Assess for malaria.
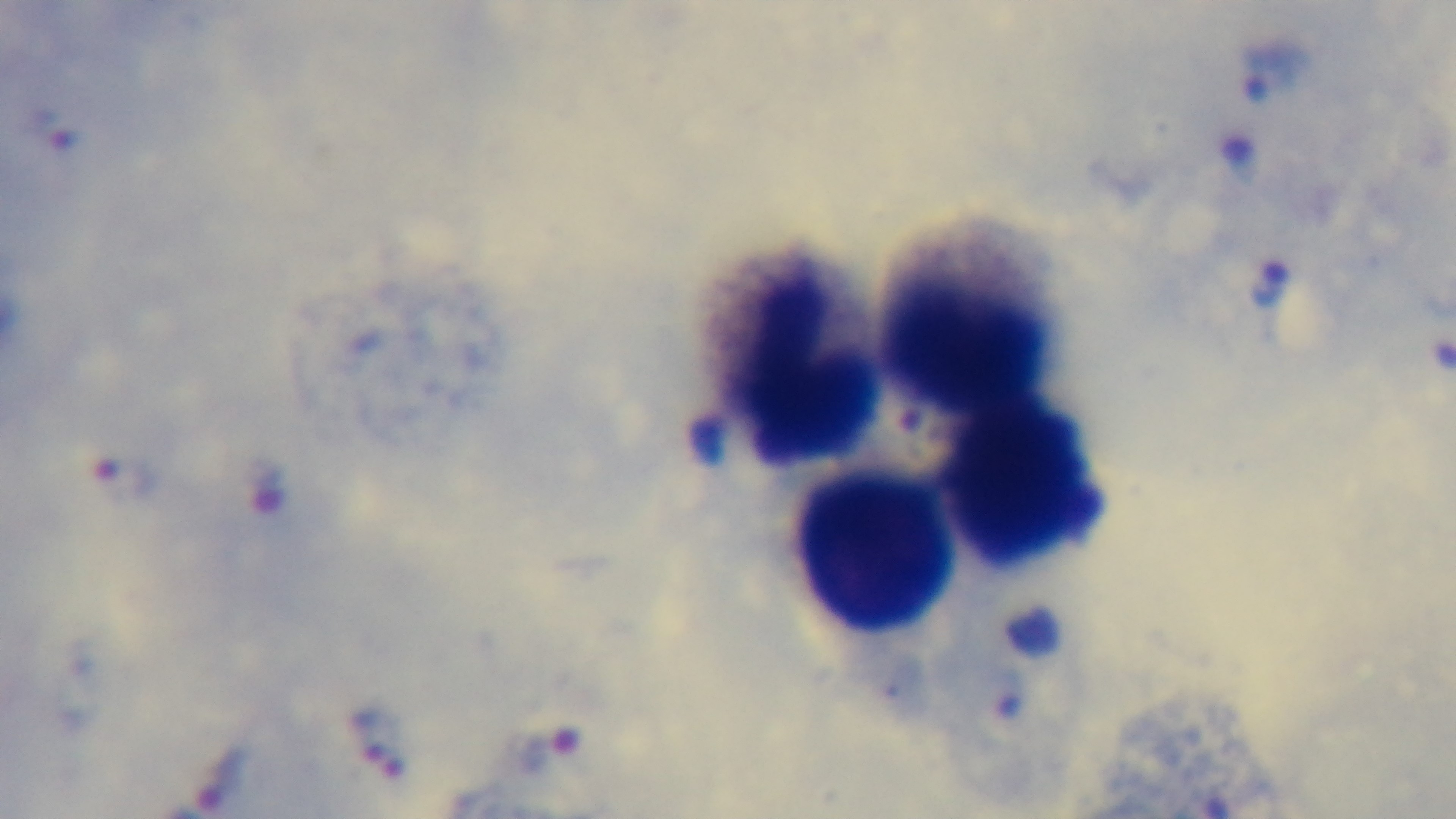

It is infected.

capture = mounted 4K digital camera
modality = light microscopy
preparation = thick
objective = 100x oil immersion
stain = Giemsa
field of view = single